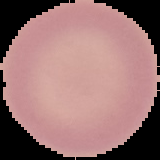
image_size: 160×160 pixels
preparation: thin blood smear
malaria_status: uninfected
image_type: segmented cell region with the area outside set to black